Outline each Trypanosoma brucei.
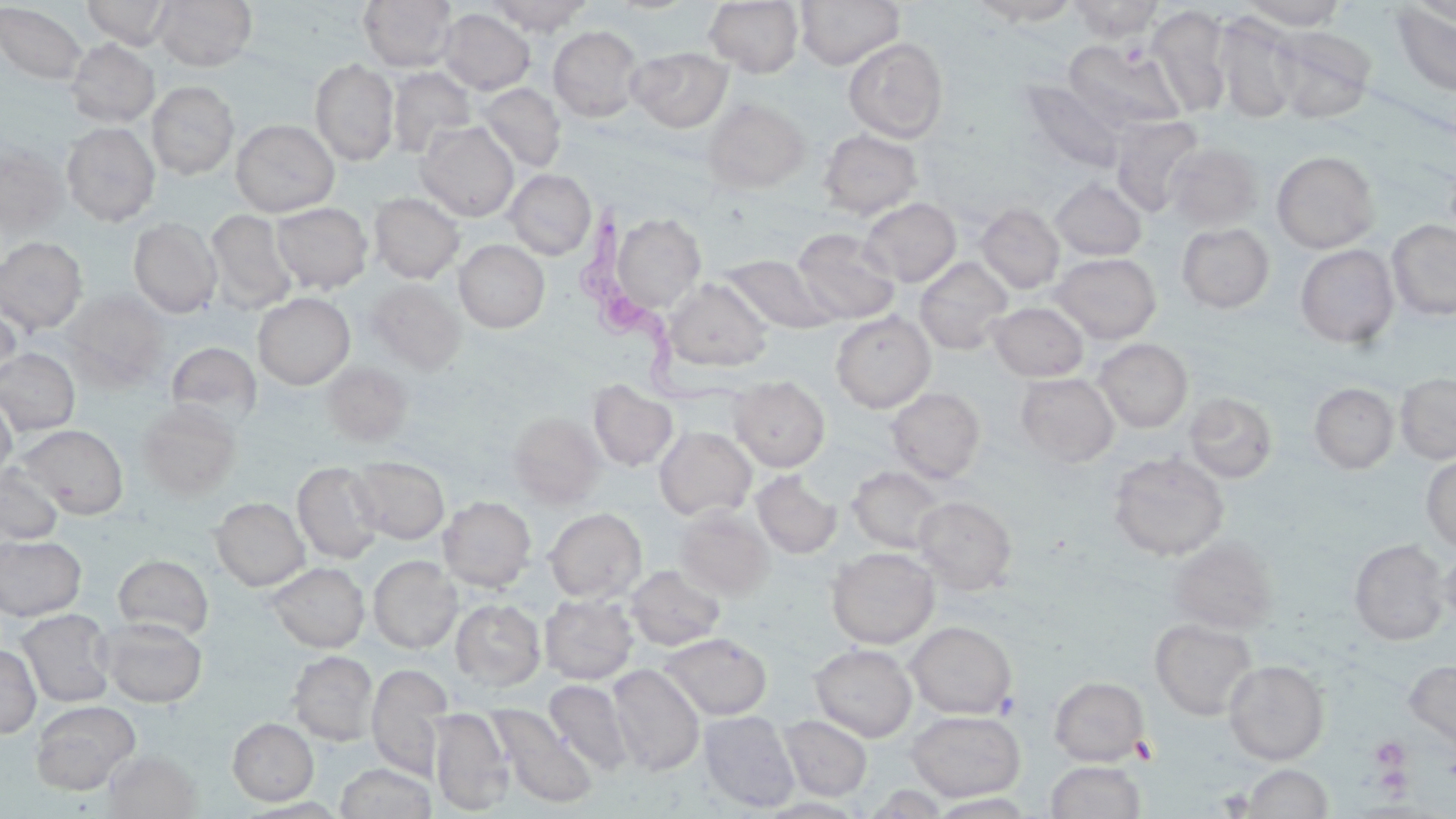
Approximate bounding boxes as named x1/y1/x2/y2 corners in pixels.
Trypanosoma brucei: (x1=575, y1=207, x2=745, y2=412).

Uninfected red blood cell locations: (x1=81, y1=0, x2=176, y2=49), (x1=154, y1=0, x2=257, y2=71), (x1=358, y1=0, x2=458, y2=73), (x1=488, y1=0, x2=593, y2=35), (x1=604, y1=0, x2=700, y2=15), (x1=795, y1=0, x2=904, y2=69), (x1=1067, y1=0, x2=1164, y2=42), (x1=1240, y1=0, x2=1349, y2=30), (x1=704, y1=1, x2=804, y2=77), (x1=969, y1=1, x2=1082, y2=26), (x1=1390, y1=2, x2=1456, y2=99), (x1=0, y1=3, x2=88, y2=85), (x1=1146, y1=5, x2=1233, y2=116), (x1=438, y1=8, x2=536, y2=95), (x1=1214, y1=14, x2=1301, y2=123), (x1=1269, y1=25, x2=1377, y2=123), (x1=548, y1=26, x2=644, y2=122), (x1=842, y1=37, x2=948, y2=142), (x1=65, y1=38, x2=160, y2=127), (x1=1064, y1=40, x2=1186, y2=133), (x1=628, y1=46, x2=733, y2=133), (x1=310, y1=58, x2=399, y2=166), (x1=386, y1=66, x2=477, y2=158), (x1=1018, y1=79, x2=1127, y2=174), (x1=147, y1=81, x2=239, y2=179), (x1=477, y1=83, x2=566, y2=172), (x1=703, y1=97, x2=810, y2=193), (x1=1110, y1=116, x2=1205, y2=216), (x1=231, y1=119, x2=339, y2=216), (x1=61, y1=122, x2=160, y2=225), (x1=416, y1=122, x2=519, y2=221), (x1=818, y1=128, x2=923, y2=219), (x1=0, y1=143, x2=68, y2=236), (x1=1165, y1=143, x2=1263, y2=230), (x1=1272, y1=151, x2=1379, y2=253), (x1=505, y1=169, x2=596, y2=260), (x1=1051, y1=178, x2=1147, y2=260), (x1=369, y1=192, x2=465, y2=283), (x1=859, y1=198, x2=961, y2=286), (x1=271, y1=202, x2=372, y2=294), (x1=976, y1=203, x2=1064, y2=294), (x1=206, y1=209, x2=297, y2=314), (x1=608, y1=212, x2=707, y2=314), (x1=128, y1=217, x2=221, y2=318), (x1=1386, y1=219, x2=1456, y2=321), (x1=1176, y1=223, x2=1274, y2=313), (x1=792, y1=228, x2=900, y2=324), (x1=0, y1=236, x2=88, y2=335), (x1=454, y1=240, x2=549, y2=333), (x1=1295, y1=244, x2=1399, y2=348), (x1=1050, y1=252, x2=1161, y2=343), (x1=720, y1=253, x2=837, y2=333), (x1=915, y1=257, x2=1013, y2=355), (x1=664, y1=277, x2=772, y2=372), (x1=366, y1=279, x2=465, y2=374), (x1=62, y1=290, x2=170, y2=386), (x1=253, y1=293, x2=355, y2=389), (x1=0, y1=300, x2=22, y2=385), (x1=988, y1=301, x2=1088, y2=381), (x1=831, y1=311, x2=936, y2=413), (x1=1094, y1=338, x2=1193, y2=432), (x1=166, y1=342, x2=261, y2=429), (x1=0, y1=347, x2=81, y2=435), (x1=322, y1=362, x2=412, y2=446), (x1=1395, y1=372, x2=1456, y2=464), (x1=1016, y1=373, x2=1119, y2=467), (x1=730, y1=376, x2=830, y2=472), (x1=589, y1=380, x2=677, y2=471), (x1=1309, y1=383, x2=1399, y2=474), (x1=886, y1=387, x2=986, y2=483), (x1=1184, y1=392, x2=1278, y2=484), (x1=0, y1=395, x2=17, y2=481), (x1=137, y1=401, x2=241, y2=499), (x1=509, y1=411, x2=606, y2=507), (x1=19, y1=424, x2=129, y2=518), (x1=654, y1=426, x2=756, y2=520), (x1=1108, y1=451, x2=1229, y2=561), (x1=1421, y1=453, x2=1456, y2=554), (x1=349, y1=456, x2=449, y2=543), (x1=292, y1=462, x2=385, y2=562), (x1=0, y1=464, x2=64, y2=547), (x1=848, y1=466, x2=945, y2=554), (x1=752, y1=471, x2=841, y2=558), (x1=438, y1=496, x2=536, y2=591), (x1=914, y1=496, x2=1017, y2=595), (x1=211, y1=498, x2=309, y2=591), (x1=674, y1=506, x2=774, y2=600), (x1=544, y1=508, x2=646, y2=603), (x1=0, y1=535, x2=87, y2=621), (x1=1167, y1=536, x2=1279, y2=634), (x1=1348, y1=539, x2=1450, y2=645), (x1=1438, y1=544, x2=1456, y2=633), (x1=827, y1=547, x2=939, y2=649), (x1=113, y1=554, x2=214, y2=639), (x1=368, y1=556, x2=461, y2=653), (x1=266, y1=562, x2=369, y2=652), (x1=626, y1=565, x2=726, y2=650), (x1=540, y1=593, x2=638, y2=684), (x1=451, y1=599, x2=546, y2=690), (x1=17, y1=608, x2=116, y2=707), (x1=100, y1=617, x2=208, y2=707), (x1=1150, y1=618, x2=1258, y2=720), (x1=906, y1=621, x2=1016, y2=719), (x1=659, y1=632, x2=772, y2=720), (x1=0, y1=644, x2=41, y2=738), (x1=810, y1=644, x2=917, y2=741), (x1=288, y1=650, x2=378, y2=745), (x1=1404, y1=659, x2=1456, y2=752), (x1=1224, y1=660, x2=1329, y2=764), (x1=366, y1=663, x2=453, y2=781), (x1=608, y1=664, x2=705, y2=776), (x1=1049, y1=676, x2=1150, y2=766), (x1=544, y1=678, x2=634, y2=777), (x1=31, y1=700, x2=140, y2=795), (x1=489, y1=705, x2=597, y2=809), (x1=430, y1=708, x2=514, y2=815), (x1=906, y1=710, x2=1026, y2=802), (x1=699, y1=711, x2=800, y2=812), (x1=779, y1=715, x2=872, y2=801), (x1=227, y1=718, x2=318, y2=805), (x1=103, y1=750, x2=201, y2=818), (x1=1045, y1=760, x2=1147, y2=819), (x1=335, y1=762, x2=437, y2=819), (x1=1242, y1=764, x2=1332, y2=818). Platelet locations: (x1=1371, y1=737, x2=1410, y2=770). Slide-level diagnosis: Trypanosoma brucei. Thin blood smear. 1000x magnification. Single field of view. May-Grünwald-Giemsa-stained preparation. Light microscopy. Image is 1456×819 pixels.